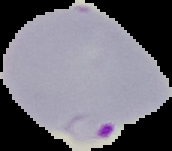
From a thin blood smear. Result: Plasmodium parasites detected. Cell region segmented out of the field of view; the surrounding area is masked to black. Image is 172×151 pixels.